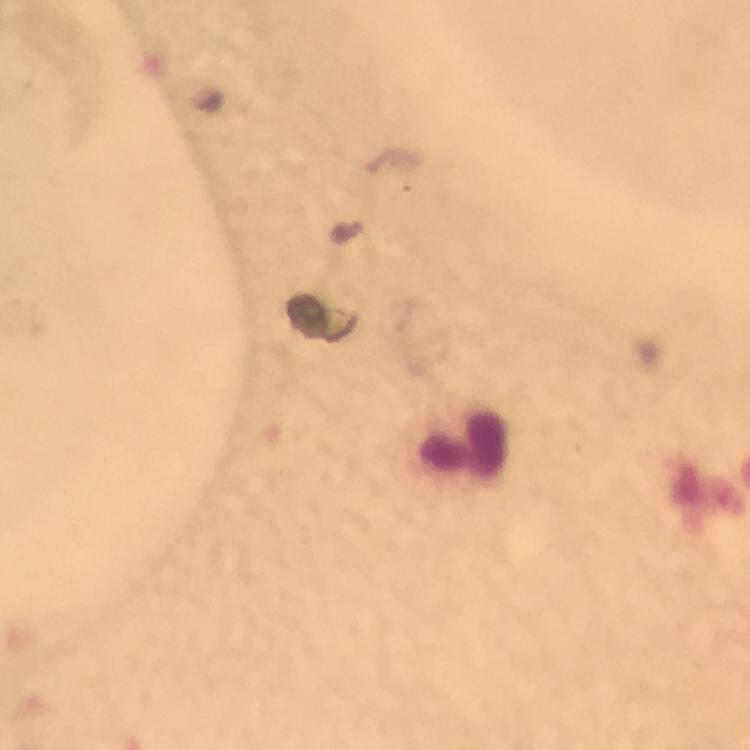

stain: Giemsa
cropped_from: a single field of view
leukocyte_locations: 'approximate centers as (x, y) in pixels: (463, 446)'
immersion_oil: applied
magnification: 100x
context: from a diagnostic examination for malaria
plasmodium_parasites: none detected
image_size: 750×750 pixels
preparation: thick blood smear
capture: smartphone camera through the microscope